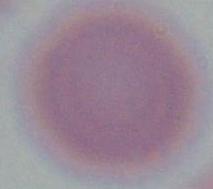

Summary:
  - Identification: red blood cell
  - Magnification: 1000x
  - Modality: micrograph